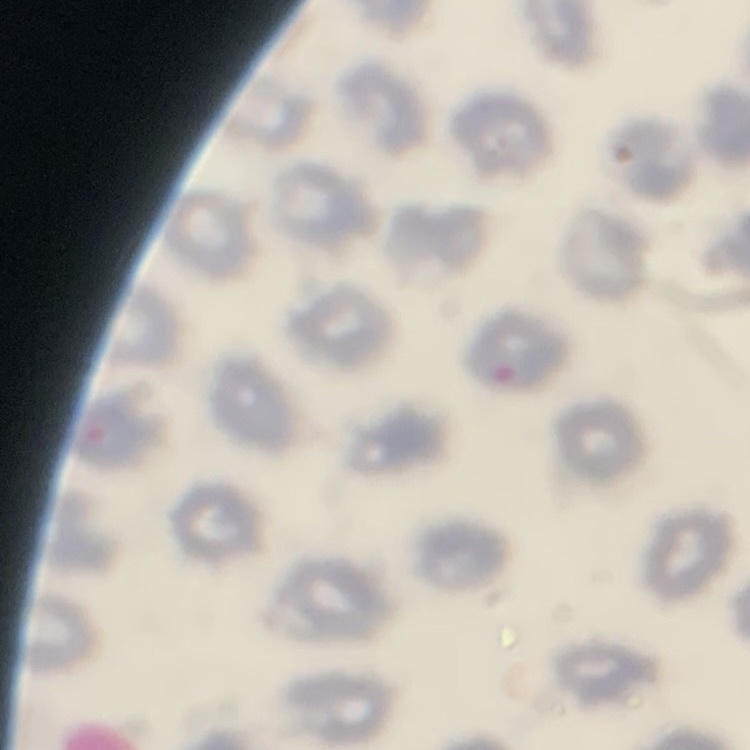

red blood cell morphology = no rouleaux formation
stain = Field's or Giemsa
image type = square crop of a larger photomicrograph
preparation = thin blood smear